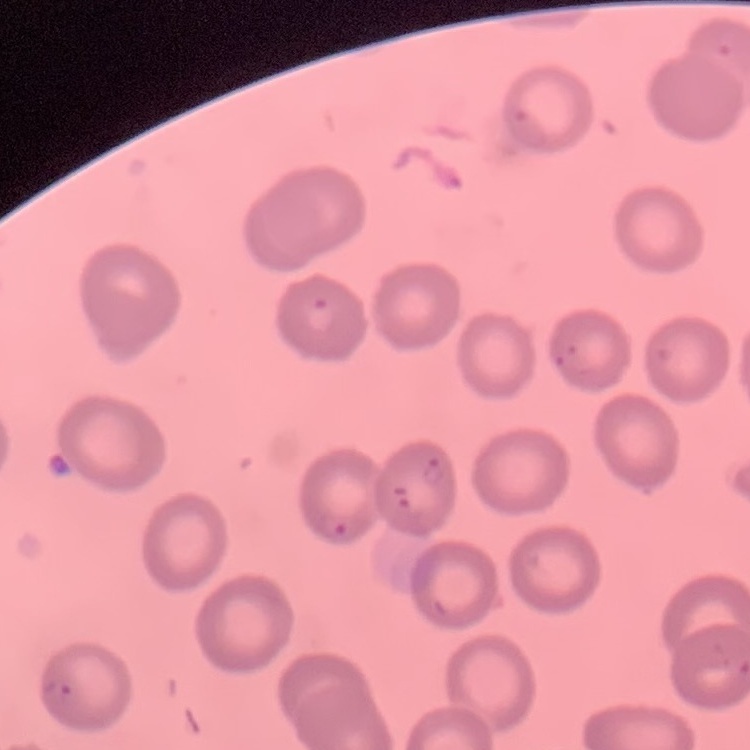

Summary:
  - Red blood cell morphology: no rouleaux formation
  - Preparation: thin peripheral smear
  - Stain: Field's or Giemsa
  - Image type: one tile cut from a larger photomicrograph